Identify the parasite.
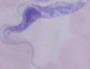

This is a trypanosome.

modality = photomicrograph
magnification = 1000x